Locate and identify every blood parasite.
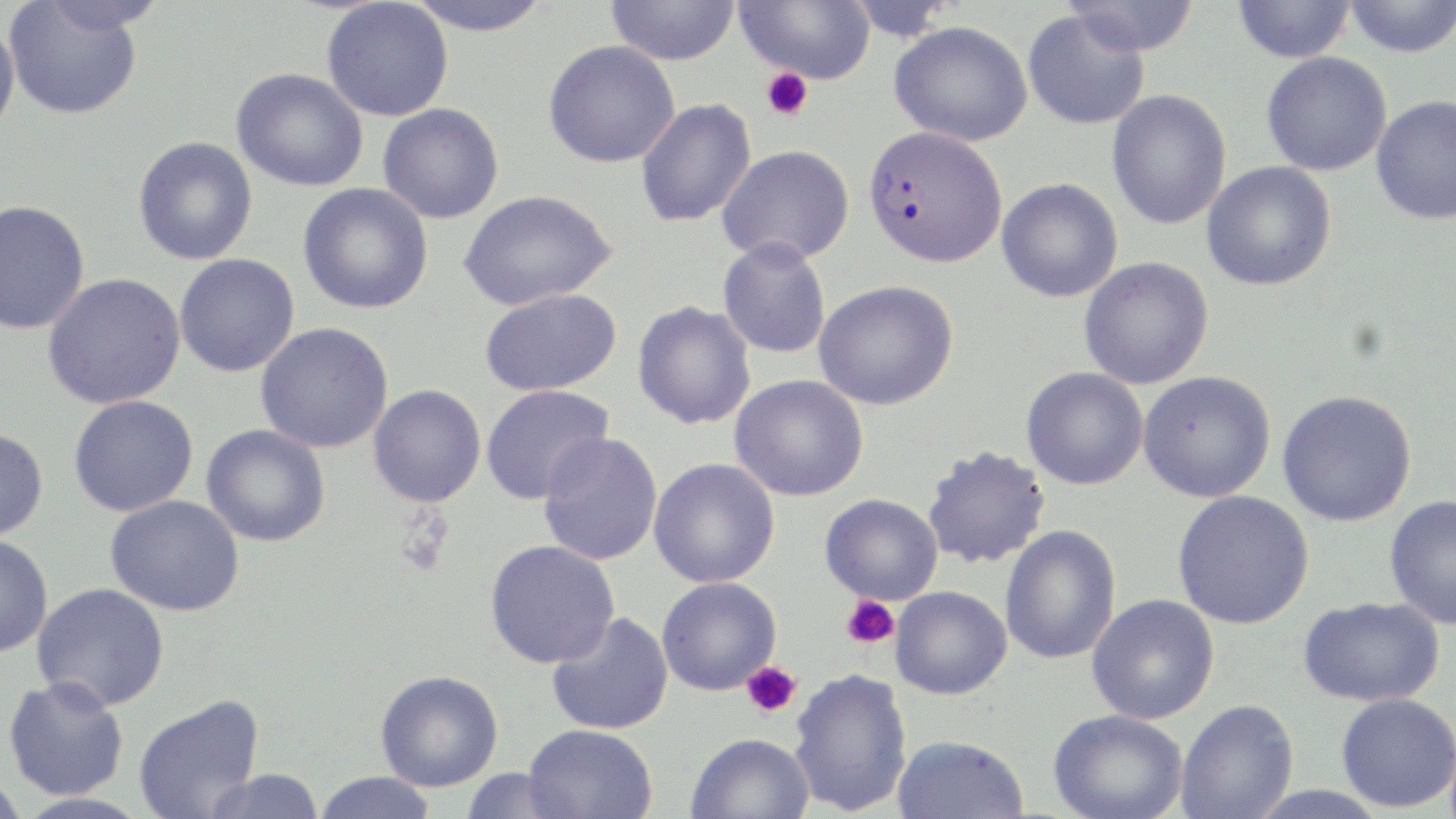
Approximate bounding boxes as (x1, y1, x2, y2) in pixels.
Plasmodium falciparum-infected red blood cells: (864, 124, 1006, 269).
No Plasmodium ovale, Plasmodium malariae, Plasmodium vivax, Babesia divergens, or Trypanosoma brucei observed.

slide-level diagnosis = Plasmodium falciparum
image size = 1456×819 pixels
preparation = thin blood film
field of view = single
stain = May-Grünwald-Giemsa
platelet locations = approximate bounding boxes as (x1, y1, x2, y2) in pixels: (762, 68, 813, 121), (841, 596, 899, 649), (741, 661, 801, 717)
magnification = 1000x
modality = optical microscopy
uninfected red blood cell locations = approximate bounding boxes as (x1, y1, x2, y2) in pixels: (402, 0, 554, 36), (734, 0, 875, 83), (1062, 0, 1200, 58), (1343, 0, 1456, 58), (4, 1, 144, 120), (321, 1, 453, 122), (606, 1, 739, 65), (1232, 1, 1355, 63), (1023, 10, 1149, 131), (0, 18, 20, 142), (889, 21, 1033, 146), (543, 40, 681, 167), (1261, 52, 1391, 176), (231, 68, 369, 192), (1106, 90, 1232, 230), (1370, 95, 1456, 225), (635, 99, 756, 227), (377, 103, 504, 224), (132, 136, 258, 265), (717, 144, 855, 265), (1202, 162, 1336, 291), (996, 178, 1123, 302), (297, 183, 433, 314), (458, 189, 617, 311), (0, 201, 90, 335), (717, 236, 831, 358), (174, 253, 300, 377), (1078, 257, 1214, 390), (42, 273, 186, 410), (814, 280, 959, 410), (478, 288, 621, 396), (633, 301, 756, 430), (255, 322, 394, 453), (1021, 367, 1148, 490), (1137, 370, 1276, 503), (730, 374, 868, 502), (368, 384, 486, 507), (481, 384, 614, 504), (1277, 389, 1417, 527), (68, 395, 199, 517), (201, 424, 331, 547), (0, 427, 49, 541), (538, 432, 663, 566), (922, 445, 1050, 570), (649, 458, 780, 588), (1172, 490, 1314, 630), (820, 493, 943, 604), (1384, 494, 1456, 630), (105, 495, 244, 616), (1000, 525, 1122, 665), (0, 534, 53, 658), (484, 539, 620, 668), (657, 577, 781, 695), (32, 582, 170, 712), (890, 586, 1012, 699), (1086, 594, 1219, 724), (1297, 596, 1445, 707), (546, 611, 673, 735), (789, 668, 912, 816), (375, 669, 503, 791), (3, 676, 129, 801), (1335, 692, 1456, 812), (133, 694, 265, 819), (1175, 699, 1299, 819), (1048, 709, 1188, 819), (523, 723, 657, 818), (685, 732, 816, 819), (891, 735, 1030, 819), (200, 768, 326, 819), (458, 768, 576, 818), (313, 771, 438, 819), (0, 772, 28, 819)